Evaluate for malaria.
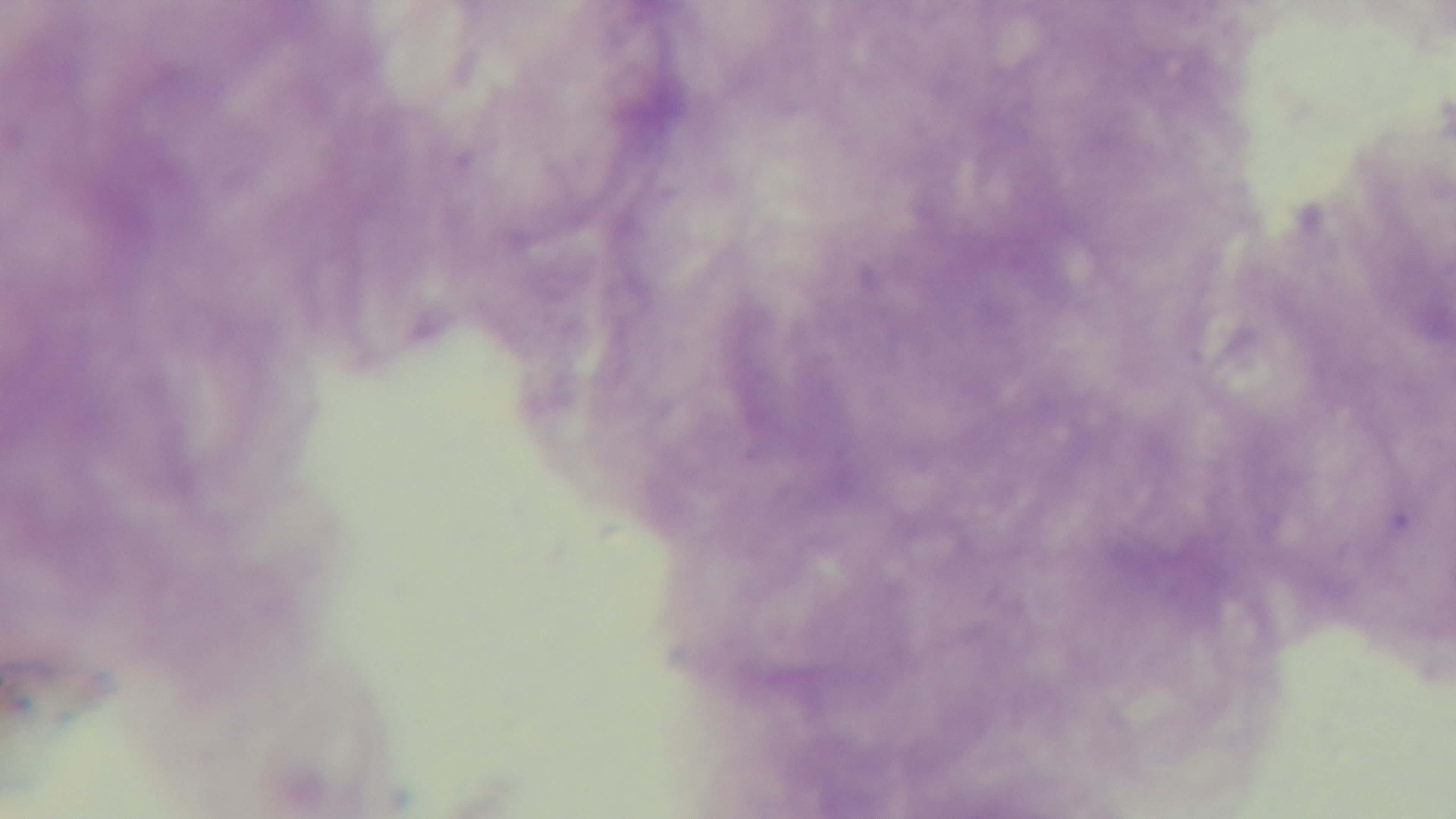

It is uninfected.

Preparation: thick blood film. One field from the slide. Giemsa-stained. Captured with a mounted 4K digital camera. Light microscopy. Oil-immersion objective, 100x.